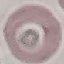 Malaria status: uninfected. Automatically extracted cell patch, resized to 64 × 64 pixels. Giemsa-stained preparation. Photographed with a smartphone camera at the microscope eyepiece. Thin blood smear.